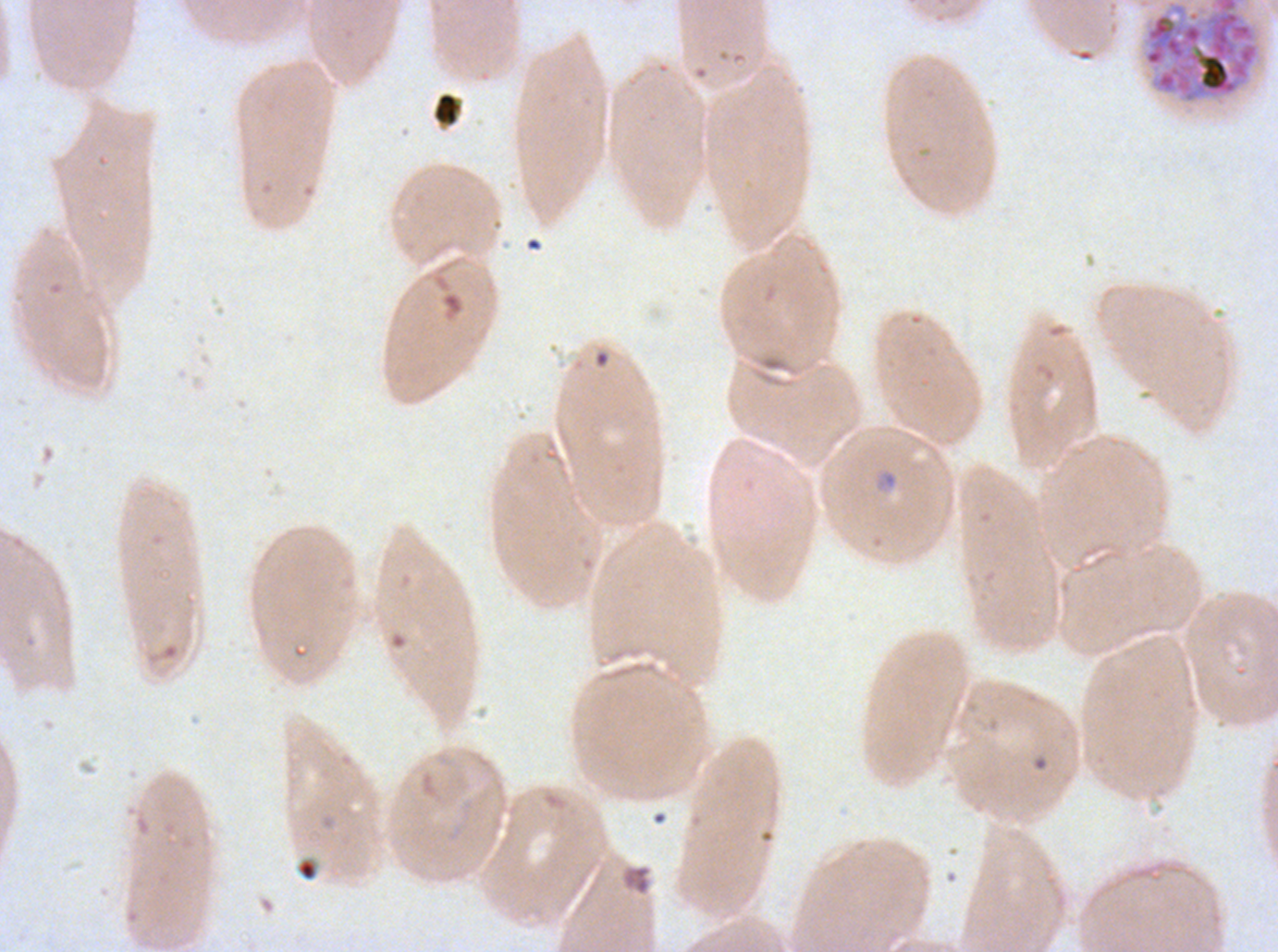

Approximate bounding boxes as {x1, y1, x2, y2} in pixels. Debris locations: {432, 92, 462, 127}. Late schizont locations: {1142, 0, 1260, 104}. Ring locations: {875, 469, 899, 491}, {416, 767, 470, 809}, {297, 859, 316, 881}. A sub-image separated from a larger composite. Giemsa-stained preparation. Ex-vivo Plasmodium falciparum culture from a patient in The Gambia, grown for 24 to 48 hours. Image is 1278×952 pixels. Life-cycle stages observed: ring, late schizont. Thin blood film.